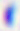

400x magnification. Photomicrograph. Toxoplasma gondii is seen.